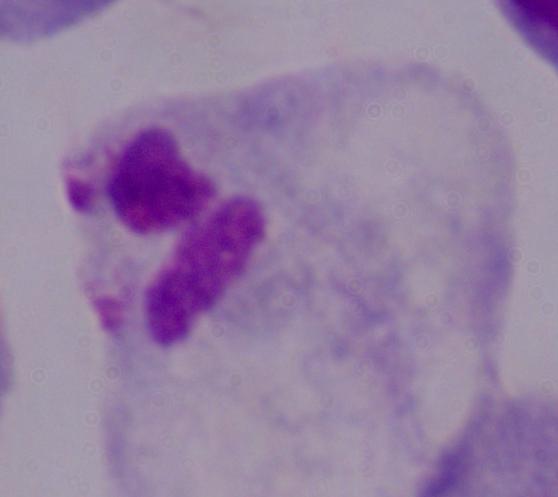

{
  "identification": "trichomonad",
  "modality": "micrograph",
  "magnification": "1000x"
}